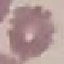
Summary:
  - Malaria status: uninfected
  - Preparation: thin blood film
  - Stain: Giemsa
  - Image type: automatically extracted cell patch, resized to 64 × 64 pixels
  - Capture: smartphone camera at the microscope eyepiece